Name the parasite shown.
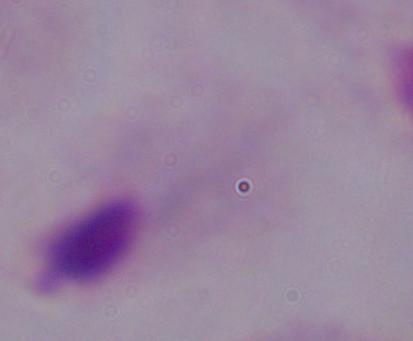

This is a trichomonad.

1000x magnification. Micrograph.